Identify the blood parasite species.
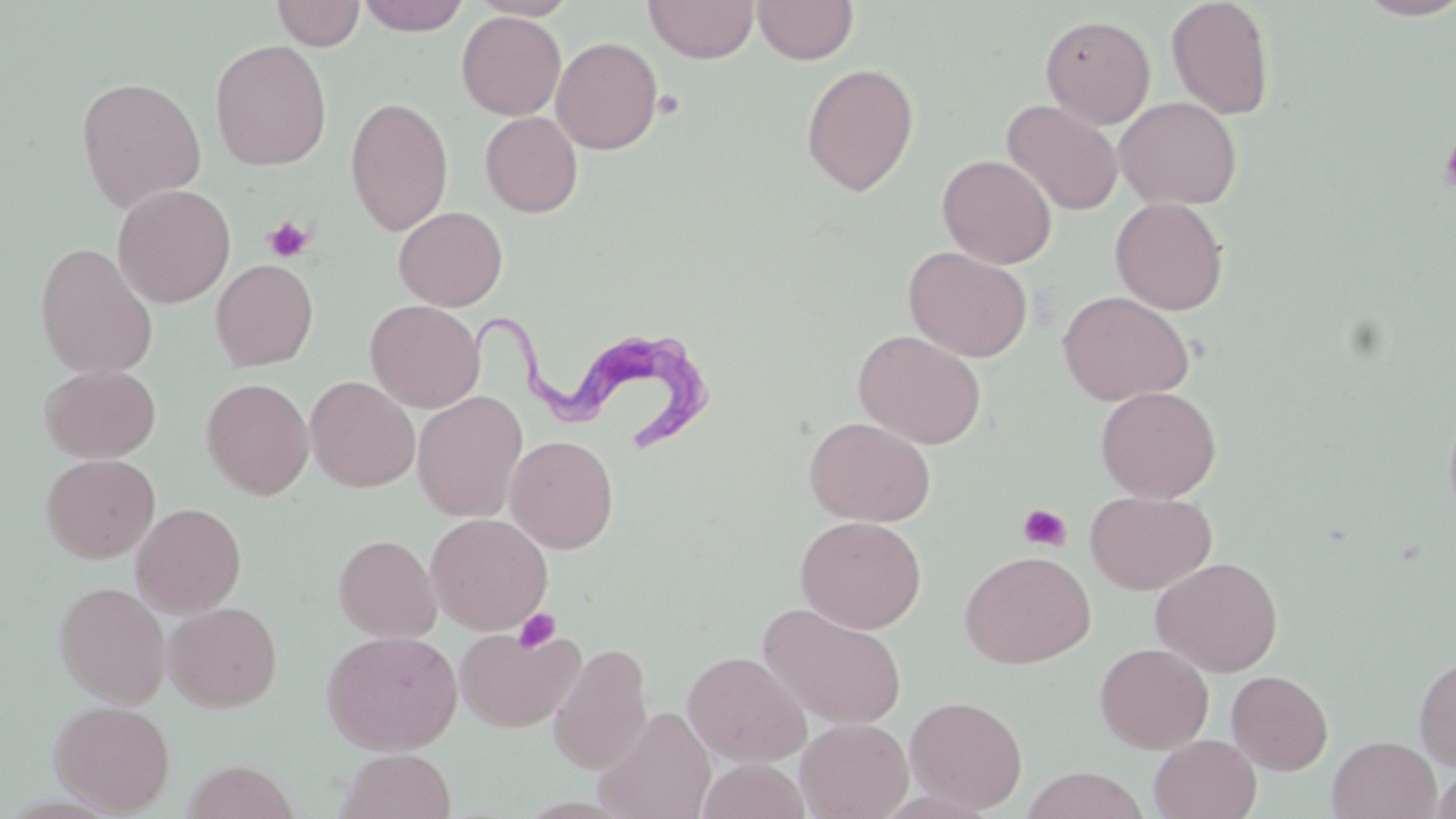
Trypanosoma brucei.

Approximate bounding boxes as (x1, y1, x2, y2) in pixels. Trypanosoma brucei locations: (472, 294, 717, 455). Uninfected red blood cell locations: (271, 0, 365, 51), (355, 0, 472, 36), (469, 0, 581, 21), (644, 0, 758, 63), (752, 0, 859, 65), (1165, 0, 1276, 120), (1354, 0, 1456, 21), (456, 11, 566, 120), (1040, 14, 1156, 129), (550, 36, 663, 155), (209, 39, 332, 171), (801, 63, 919, 196), (75, 75, 207, 212), (345, 96, 454, 237), (1115, 96, 1242, 210), (1001, 99, 1122, 216), (480, 111, 583, 218), (937, 154, 1057, 269), (113, 184, 235, 308), (1110, 196, 1229, 315), (394, 206, 508, 311), (34, 241, 159, 379), (903, 246, 1033, 362), (211, 259, 318, 371), (1057, 290, 1194, 406), (365, 300, 484, 412), (853, 329, 987, 449), (39, 364, 161, 463), (305, 376, 420, 492), (202, 377, 315, 500), (1096, 385, 1221, 503), (412, 391, 528, 522), (1441, 401, 1456, 527), (803, 416, 936, 527), (505, 435, 619, 554), (41, 453, 161, 563), (1085, 490, 1217, 595), (131, 502, 247, 616), (426, 512, 553, 635), (795, 515, 926, 633), (333, 533, 442, 643), (960, 550, 1096, 668), (1151, 556, 1284, 677), (54, 581, 171, 706), (163, 601, 283, 711), (759, 602, 908, 730), (455, 627, 584, 733), (321, 630, 463, 754), (548, 642, 653, 776), (1094, 642, 1213, 753), (682, 650, 812, 766), (1414, 653, 1456, 771), (1227, 670, 1333, 775), (904, 694, 1028, 813), (50, 700, 175, 814), (595, 705, 715, 819), (795, 717, 913, 819), (1149, 735, 1261, 819), (1327, 735, 1441, 819), (336, 749, 456, 819), (181, 759, 301, 819), (699, 759, 810, 818), (1431, 765, 1456, 819), (1021, 767, 1150, 819). Platelet locations: (653, 89, 685, 120), (1440, 132, 1456, 197), (264, 216, 315, 262), (1018, 503, 1072, 552), (513, 608, 561, 653). Captured at 1000x magnification. Single field of view. Image is 1456×819 pixels. Light microscopy. Thin blood film. May-Grünwald-Giemsa stain.